Assess this cell for malaria.
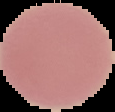

Uninfected.

image size = 115×112 pixels
image type = segmented cell region with the area outside set to black
preparation = thin blood smear